State which parasite is depicted.
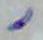

This is Toxoplasma gondii.

{
  "magnification": "1000x",
  "modality": "micrograph"
}